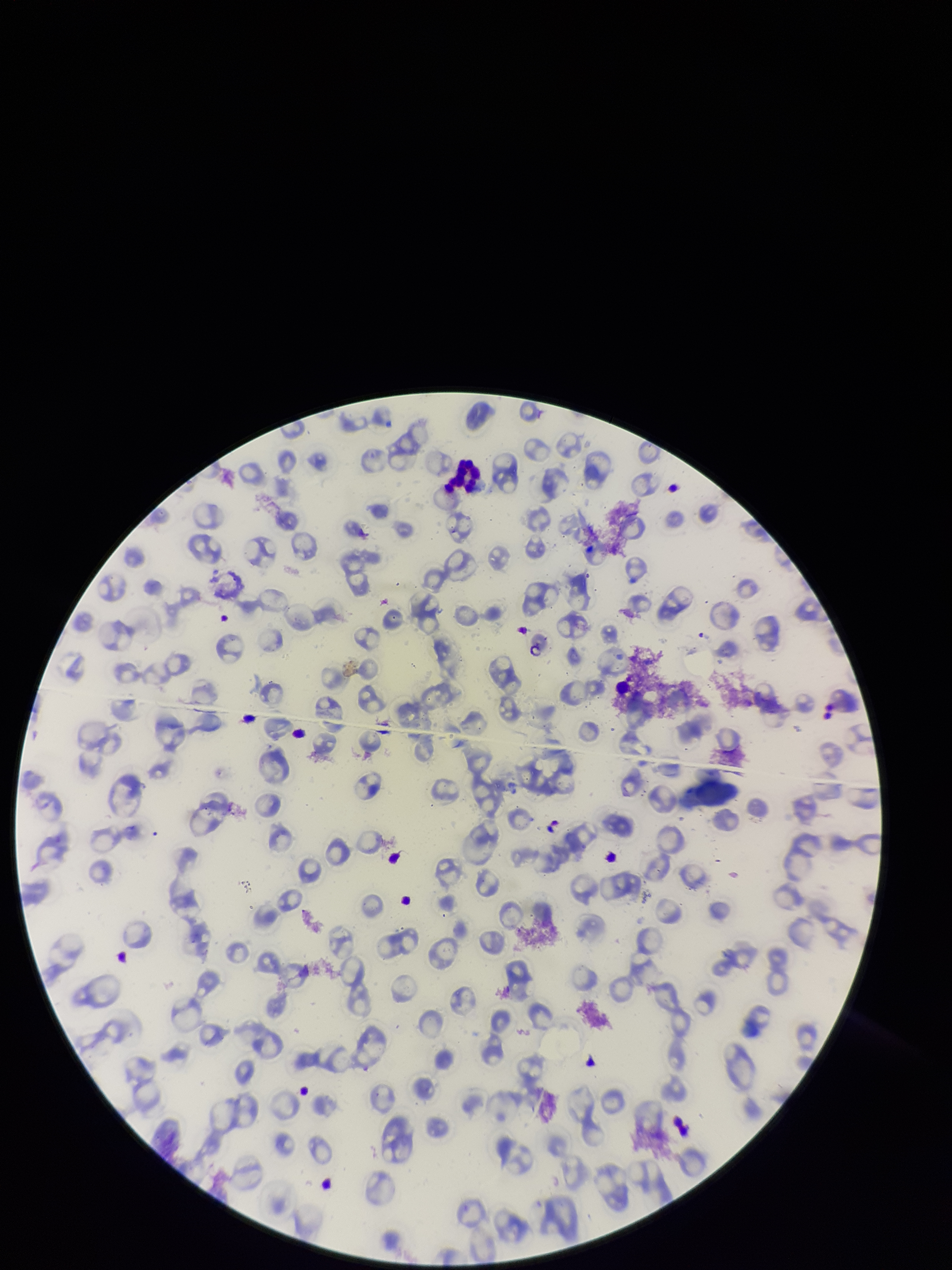 Red blood cell count: 91. Image is 952×1270 pixels. Giemsa stain. Preparation: thin. Patient malaria status: positive. Parasitized red blood cells: none detected. Single field of view. Parasitized red blood cell count: 0. Photographed through the microscope eyepiece with a smartphone camera. Species reported for this patient: Plasmodium falciparum.